Locate and identify every blood parasite.
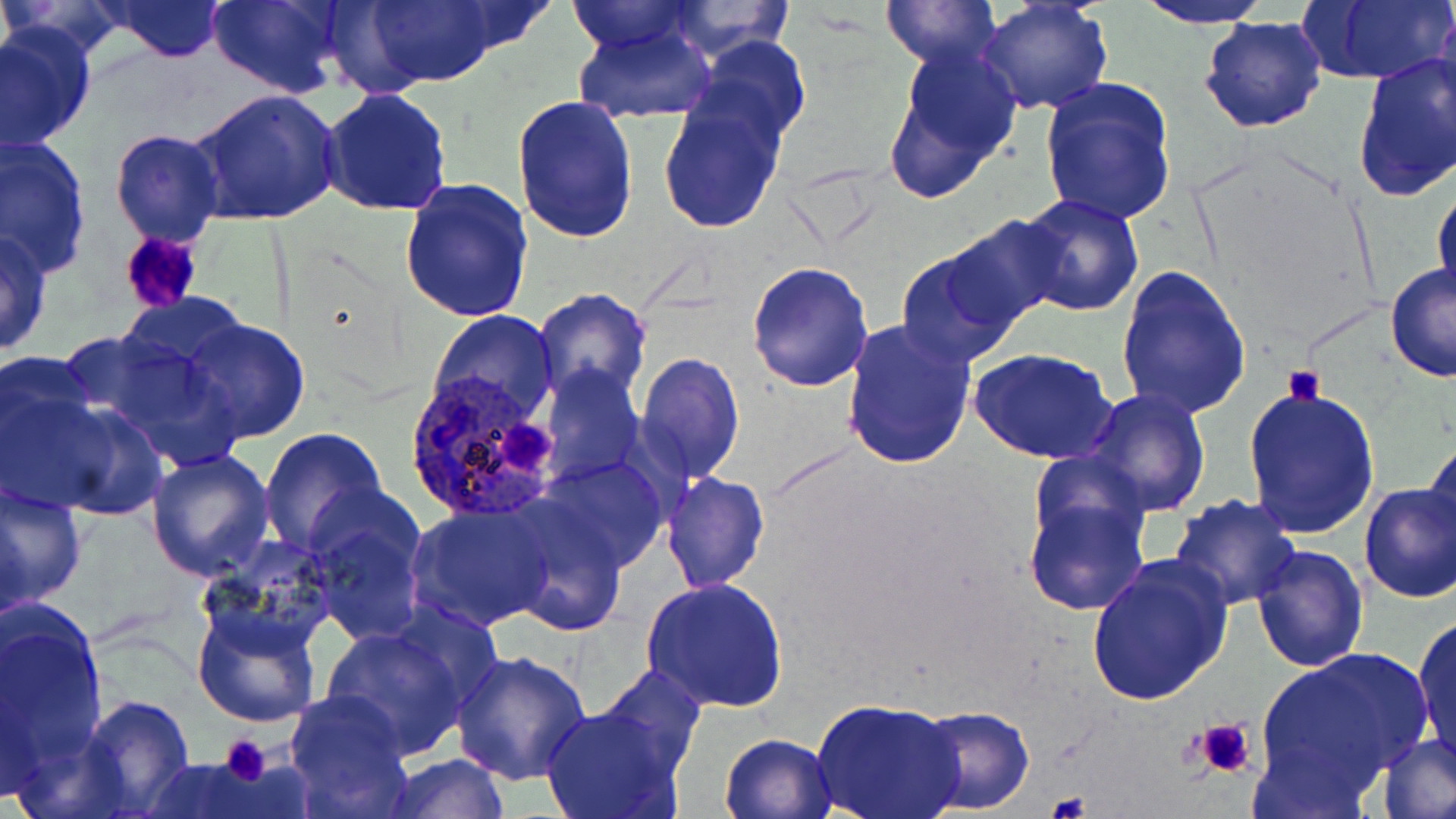

Approximate bounding boxes as (x1, y1, x2, y2) in pixels.
Plasmodium ovale-infected red blood cells: (402, 370, 563, 522).
No Plasmodium falciparum, Plasmodium malariae, Plasmodium vivax, Babesia divergens, or Trypanosoma brucei observed.

Uninfected red blood cell locations: (0, 0, 132, 64), (104, 0, 228, 61), (206, 0, 346, 97), (361, 0, 504, 88), (882, 0, 1000, 71), (1297, 0, 1455, 87), (563, 1, 706, 56), (660, 1, 797, 59), (977, 1, 1113, 115), (1135, 1, 1276, 29), (1434, 6, 1456, 122), (1200, 14, 1326, 133), (572, 22, 718, 124), (0, 24, 95, 154), (689, 34, 812, 151), (885, 44, 1022, 196), (1352, 52, 1456, 202), (1038, 78, 1178, 225), (319, 88, 452, 216), (191, 89, 343, 225), (658, 92, 787, 234), (512, 93, 639, 243), (109, 129, 224, 247), (1, 135, 94, 276), (399, 177, 534, 323), (1432, 184, 1456, 304), (1016, 193, 1143, 316), (941, 214, 1072, 332), (0, 228, 53, 358), (895, 248, 1025, 369), (746, 261, 875, 392), (1384, 264, 1456, 382), (1116, 266, 1251, 421), (531, 287, 653, 408), (116, 291, 252, 386), (430, 309, 557, 428), (839, 318, 977, 470), (181, 319, 310, 443), (79, 331, 252, 472), (971, 348, 1119, 463), (0, 350, 105, 510), (634, 351, 744, 483), (539, 365, 642, 485), (1242, 385, 1381, 540), (18, 387, 168, 523), (1081, 388, 1212, 517), (258, 428, 388, 556), (1422, 437, 1454, 552), (146, 448, 276, 581), (536, 456, 671, 573), (662, 472, 768, 593), (1021, 478, 1152, 617), (0, 480, 87, 612), (1358, 484, 1456, 603), (1168, 493, 1298, 610), (0, 497, 29, 630), (303, 497, 428, 645), (498, 499, 630, 638), (408, 504, 556, 631), (194, 538, 335, 664), (1251, 544, 1369, 672), (1084, 556, 1234, 708), (641, 576, 787, 713), (1, 604, 108, 780), (192, 605, 321, 728), (1411, 613, 1456, 764), (321, 625, 473, 760), (451, 648, 591, 786), (1256, 648, 1433, 795), (595, 665, 707, 776), (0, 674, 44, 809), (286, 692, 415, 818), (79, 695, 196, 818), (811, 697, 965, 819), (913, 704, 1035, 815), (540, 705, 686, 819), (719, 732, 838, 819), (1375, 734, 1456, 819), (384, 753, 510, 817), (139, 758, 272, 818). Platelet locations: (118, 231, 203, 315), (1283, 364, 1324, 405), (499, 421, 558, 479), (1193, 717, 1258, 781), (217, 735, 271, 786), (1047, 791, 1092, 819). Slide-level diagnosis: Plasmodium ovale. Single field of view. May-Grünwald-Giemsa-stained preparation. Image is 1456×819 pixels. Optical microscopy. 1000x magnification. Thin blood smear.